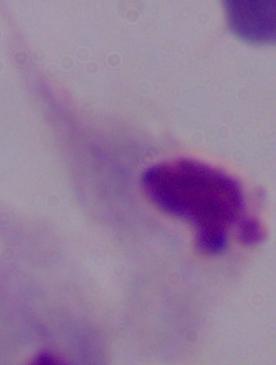 A trichomonad is seen. Captured at 1000x magnification. Photomicrograph.